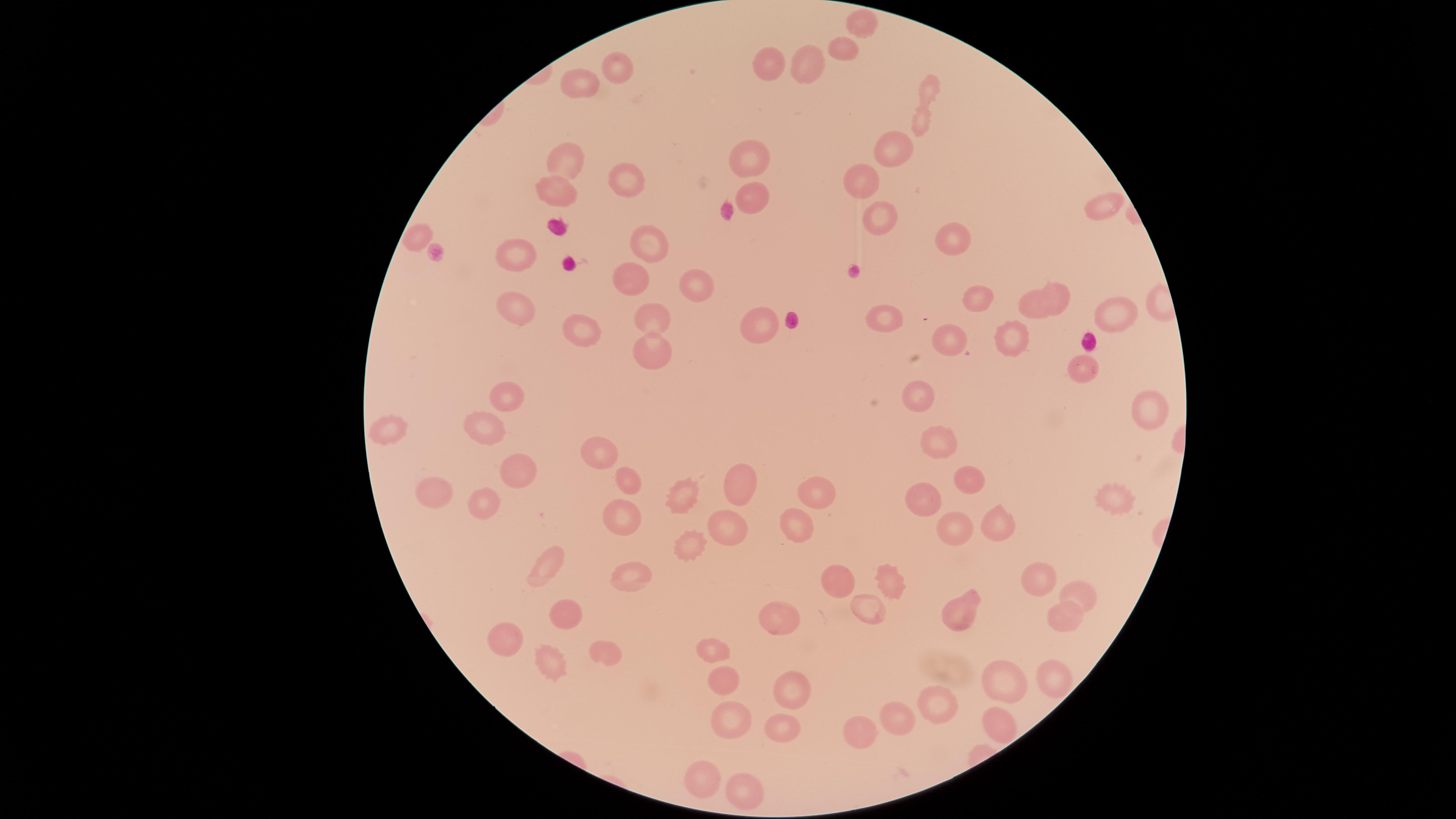 Approximate marker points as (x, y) in pixels. Uninfected RBCs: (860, 17), (840, 48), (805, 63), (772, 64), (615, 66), (931, 84), (567, 88), (917, 120), (896, 145), (746, 158), (563, 162), (857, 180), (621, 181), (554, 190), (751, 194), (1099, 204), (876, 219), (423, 233), (955, 236), (650, 245), (515, 248), (626, 278), (703, 281), (1059, 289), (975, 298), (514, 303), (1034, 303), (1111, 314), (653, 315), (886, 315), (758, 326), (581, 331), (1011, 333), (952, 337), (652, 350), (1081, 367), (916, 392), (507, 398), (1146, 408), (484, 430), (393, 433), (932, 439), (604, 446), (514, 473), (967, 476), (626, 479), (744, 479), (822, 491), (438, 492), (683, 494), (1117, 495), (924, 497), (484, 506), (619, 514), (996, 521), (794, 524), (730, 525), (960, 529), (691, 542), (546, 565), (893, 574), (1040, 574), (627, 577), (846, 583), (1080, 595), (564, 609), (867, 609), (957, 611), (1061, 612), (782, 624), (508, 635), (603, 648), (714, 648), (556, 661), (1049, 675), (721, 676), (1007, 677), (788, 685), (934, 703), (730, 714), (898, 716), (994, 720), (785, 724), (858, 730), (705, 771), (745, 791). Single field of view. Image is 1456×819 pixels. Giemsa stain. Smartphone photograph through the microscope eyepiece. Thin blood smear. Circular visible region. Presence: no malaria parasites identified.